Comment on the morphology of the red blood cells.
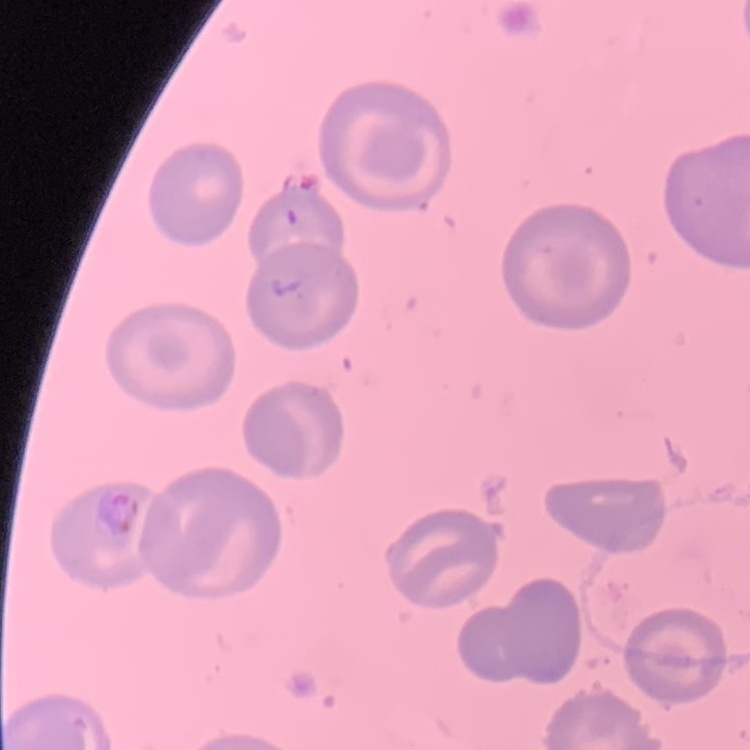

They show no rouleaux formation.

Summary:
  - Stain: Field's or Giemsa
  - Image type: square crop of a larger photomicrograph
  - Preparation: thin peripheral smear